Outline each blood parasite and name the species.
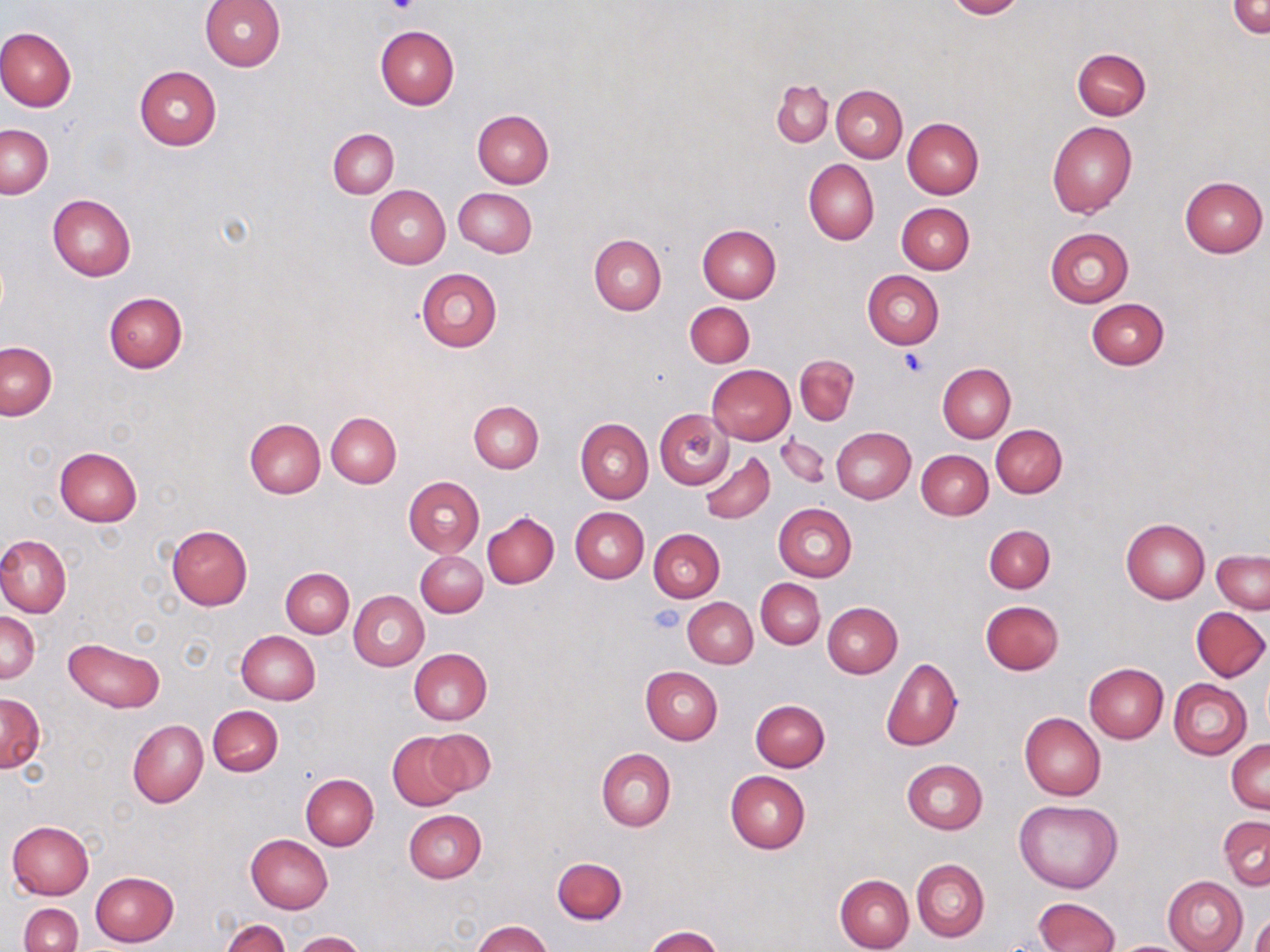
No blood parasites observed.

slide_level_diagnosis: negative for blood parasites
platelet_locations: 'approximate bounding boxes as named x1/y1/x2/y2 corners in pixels: (x1=383, y1=0, x2=419, y2=17), (x1=900, y1=348, x2=928, y2=375), (x1=650, y1=605, x2=687, y2=635)'
image_size: 1270×952 pixels
stain: May-Grünwald-Giemsa
modality: light microscopy
uninfected_red_blood_cell_locations: 'approximate bounding boxes as named x1/y1/x2/y2 corners in pixels: (x1=201, y1=0, x2=285, y2=71), (x1=945, y1=0, x2=1024, y2=19), (x1=1229, y1=1, x2=1270, y2=38), (x1=375, y1=25, x2=458, y2=110), (x1=0, y1=26, x2=76, y2=111), (x1=1072, y1=48, x2=1151, y2=120), (x1=134, y1=65, x2=222, y2=150), (x1=772, y1=80, x2=832, y2=147), (x1=831, y1=85, x2=907, y2=161), (x1=472, y1=110, x2=553, y2=188), (x1=902, y1=117, x2=984, y2=198), (x1=1047, y1=120, x2=1136, y2=218), (x1=1, y1=124, x2=53, y2=198), (x1=328, y1=129, x2=398, y2=198), (x1=804, y1=159, x2=879, y2=245), (x1=1179, y1=176, x2=1268, y2=258), (x1=366, y1=185, x2=450, y2=268), (x1=455, y1=187, x2=537, y2=256), (x1=48, y1=194, x2=136, y2=282), (x1=896, y1=201, x2=975, y2=274), (x1=698, y1=224, x2=782, y2=303), (x1=1045, y1=228, x2=1134, y2=307), (x1=589, y1=234, x2=666, y2=315), (x1=415, y1=268, x2=502, y2=352), (x1=862, y1=271, x2=943, y2=349), (x1=104, y1=291, x2=188, y2=373), (x1=1086, y1=298, x2=1170, y2=370), (x1=685, y1=301, x2=755, y2=368), (x1=1, y1=342, x2=56, y2=419), (x1=795, y1=354, x2=858, y2=425), (x1=938, y1=363, x2=1015, y2=443), (x1=707, y1=365, x2=795, y2=445), (x1=468, y1=401, x2=543, y2=472), (x1=654, y1=409, x2=733, y2=487), (x1=326, y1=411, x2=401, y2=487), (x1=244, y1=417, x2=325, y2=498), (x1=575, y1=418, x2=654, y2=504), (x1=991, y1=424, x2=1067, y2=498), (x1=831, y1=427, x2=916, y2=504), (x1=776, y1=433, x2=830, y2=490), (x1=54, y1=447, x2=143, y2=527), (x1=700, y1=449, x2=775, y2=525), (x1=917, y1=450, x2=992, y2=519), (x1=404, y1=477, x2=484, y2=556), (x1=773, y1=503, x2=856, y2=582), (x1=569, y1=507, x2=647, y2=582), (x1=482, y1=512, x2=559, y2=589), (x1=568, y1=517, x2=719, y2=587), (x1=1119, y1=518, x2=1210, y2=603), (x1=984, y1=524, x2=1055, y2=593), (x1=167, y1=525, x2=253, y2=610), (x1=648, y1=528, x2=725, y2=602), (x1=0, y1=534, x2=72, y2=617), (x1=416, y1=550, x2=487, y2=617), (x1=1212, y1=550, x2=1269, y2=613), (x1=280, y1=568, x2=354, y2=637), (x1=756, y1=579, x2=825, y2=649), (x1=348, y1=590, x2=429, y2=670), (x1=682, y1=596, x2=758, y2=668), (x1=980, y1=600, x2=1063, y2=675), (x1=822, y1=602, x2=902, y2=677), (x1=1183, y1=606, x2=1261, y2=758), (x1=1192, y1=607, x2=1269, y2=681), (x1=0, y1=612, x2=40, y2=683), (x1=235, y1=631, x2=320, y2=706), (x1=64, y1=638, x2=165, y2=712), (x1=408, y1=648, x2=491, y2=725), (x1=881, y1=657, x2=963, y2=751), (x1=1084, y1=662, x2=1169, y2=743), (x1=641, y1=666, x2=722, y2=744), (x1=1168, y1=679, x2=1251, y2=759), (x1=0, y1=693, x2=45, y2=772), (x1=751, y1=699, x2=830, y2=772), (x1=208, y1=705, x2=282, y2=776), (x1=1020, y1=713, x2=1106, y2=801), (x1=128, y1=719, x2=208, y2=808), (x1=422, y1=728, x2=496, y2=797), (x1=387, y1=732, x2=467, y2=810), (x1=1228, y1=737, x2=1270, y2=812), (x1=597, y1=748, x2=676, y2=831), (x1=901, y1=759, x2=987, y2=835), (x1=725, y1=771, x2=809, y2=854), (x1=300, y1=773, x2=379, y2=850), (x1=1013, y1=800, x2=1123, y2=893), (x1=404, y1=810, x2=486, y2=883), (x1=1218, y1=815, x2=1270, y2=889), (x1=7, y1=820, x2=95, y2=899), (x1=246, y1=835, x2=332, y2=914), (x1=552, y1=858, x2=627, y2=924), (x1=911, y1=858, x2=989, y2=942), (x1=90, y1=870, x2=179, y2=946), (x1=836, y1=874, x2=914, y2=952), (x1=1163, y1=875, x2=1248, y2=952), (x1=1032, y1=897, x2=1119, y2=952), (x1=19, y1=903, x2=84, y2=952), (x1=1250, y1=912, x2=1270, y2=952), (x1=219, y1=917, x2=291, y2=952), (x1=472, y1=920, x2=551, y2=952), (x1=645, y1=927, x2=724, y2=952), (x1=292, y1=930, x2=366, y2=951)'
preparation: thin blood film
magnification: 1000x
field_of_view: single